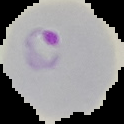
{
  "malaria_status": "parasitized",
  "preparation": "thin blood smear",
  "image_size": "124×124 pixels",
  "image_type": "segmented cell region on a black background"
}